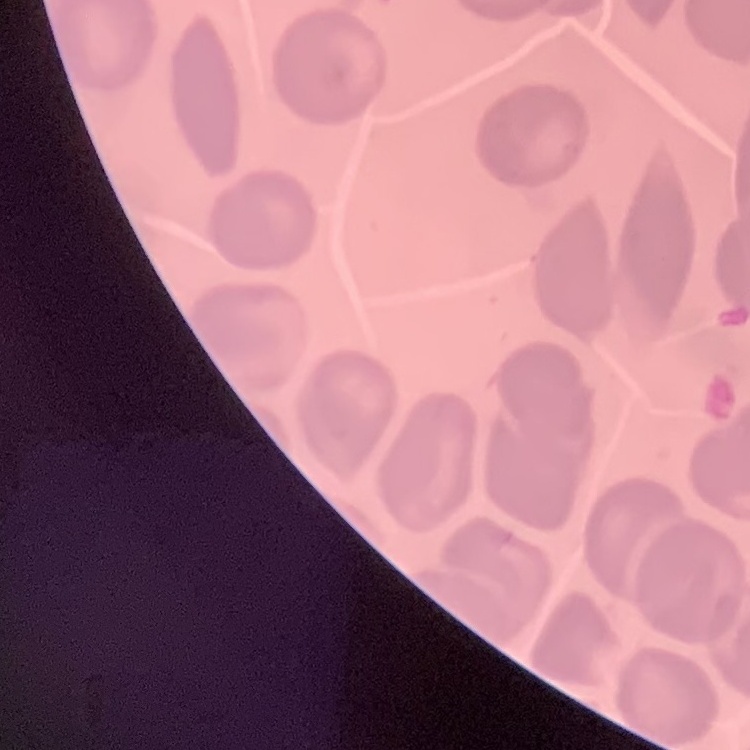
The red blood cells exhibit no rouleaux formation. Stained with either Field's or Giemsa. Square crop of a larger photomicrograph. Thin peripheral smear.